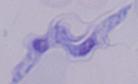
Micrograph. 1000x magnification. A trypanosome is shown.